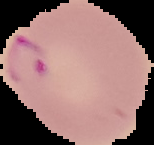

{
  "preparation": "thin blood film",
  "result": "Plasmodium parasites detected",
  "image_type": "cell region segmented out of the field of view; surrounding area masked to black",
  "image_size": "154×145 pixels"
}